Assess this cell for malaria.
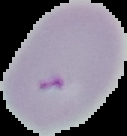

It is parasitized.

Cell region segmented out of the field of view; the surrounding area is masked to black. From a thin blood smear. Image is 127×136 pixels.